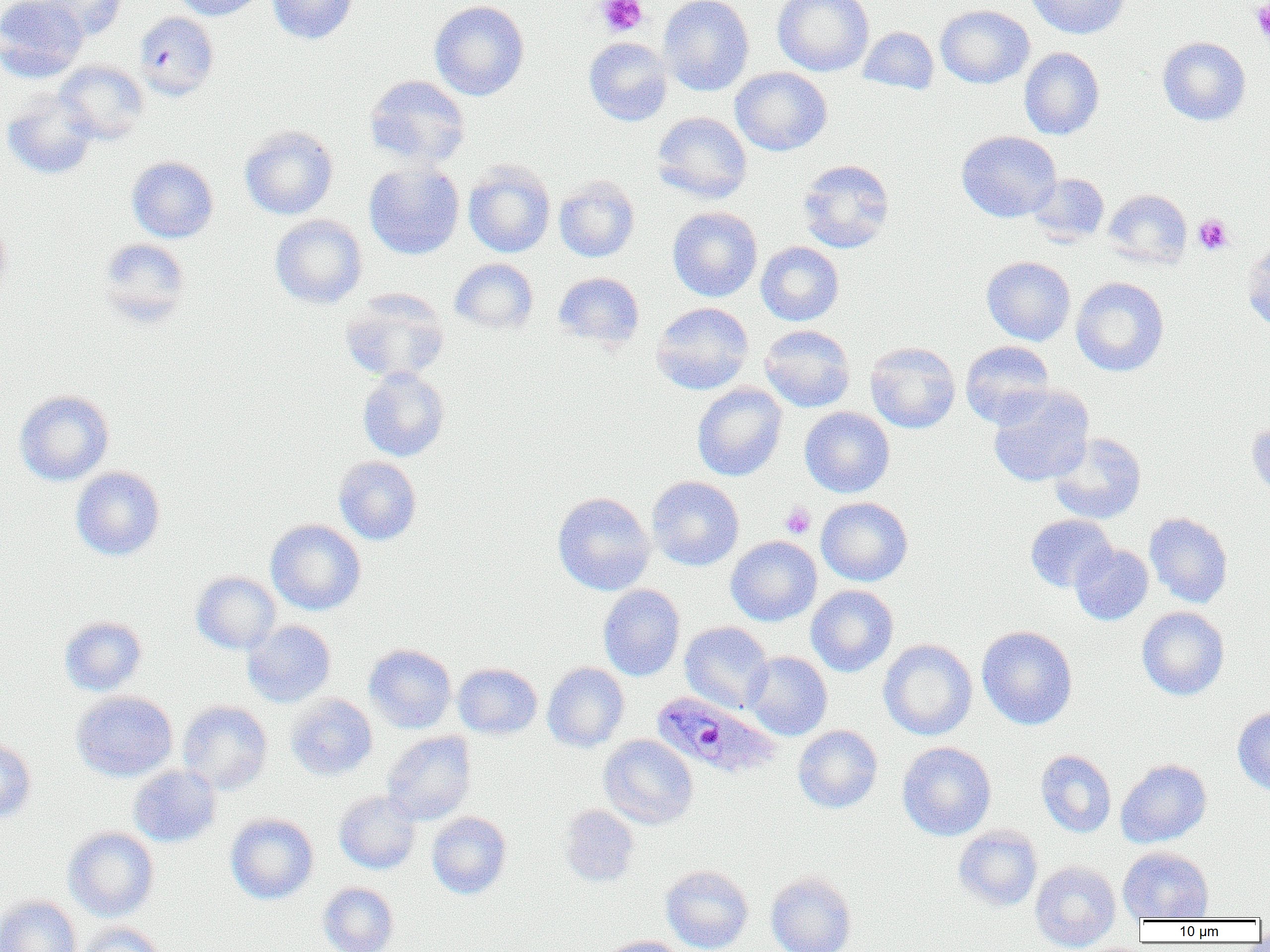
Approximate bounding boxes as (x1,y1)-(x2,y2) corner pairs in pixels. Plasmodium ovale-infected red blood cell locations: (653,691)-(782,779). Platelet locations: (597,0)-(648,37), (1251,1)-(1270,42), (1194,214)-(1232,254), (780,502)-(816,539). Uninfected red blood cell locations: (0,0)-(89,81), (34,0)-(126,40), (171,0)-(267,20), (267,0)-(358,44), (659,0)-(754,96), (773,0)-(874,76), (1026,0)-(1129,39), (429,1)-(530,101), (935,4)-(1034,89), (134,11)-(219,100), (858,26)-(939,94), (583,37)-(673,126), (1157,37)-(1251,126), (1019,48)-(1104,140), (55,61)-(150,144), (730,67)-(832,156), (363,75)-(471,168), (2,88)-(100,180), (652,112)-(752,203), (240,125)-(338,220), (957,131)-(1061,222), (126,156)-(219,243), (797,159)-(895,253), (364,161)-(465,260), (463,161)-(556,258), (1028,173)-(1110,246), (553,174)-(640,262), (1103,189)-(1192,268), (667,206)-(762,302), (269,214)-(368,309), (0,216)-(13,306), (97,238)-(191,326), (1242,240)-(1270,333), (756,242)-(844,326), (981,256)-(1076,345), (449,258)-(539,334), (553,272)-(646,350), (1071,276)-(1169,377), (339,288)-(451,383), (650,302)-(754,394), (759,324)-(855,412), (960,340)-(1056,428), (865,342)-(960,433), (357,368)-(450,462), (691,383)-(787,481), (987,387)-(1094,487), (14,390)-(114,486), (799,407)-(895,498), (1246,418)-(1270,505), (1049,433)-(1146,524), (334,456)-(421,545), (70,467)-(165,561), (647,476)-(744,571), (552,492)-(655,595), (816,497)-(912,586), (1145,513)-(1233,608), (1025,514)-(1116,592), (266,519)-(366,615), (725,536)-(822,626), (1070,542)-(1153,625), (191,571)-(281,654), (598,584)-(685,681), (806,585)-(899,676), (1137,606)-(1229,700), (59,616)-(147,696), (242,620)-(336,707), (680,622)-(773,714), (977,625)-(1078,730), (878,639)-(977,740), (364,644)-(457,733), (743,651)-(832,740), (453,662)-(542,739), (542,662)-(629,752), (72,691)-(177,781), (285,693)-(377,781), (179,699)-(377,786), (177,701)-(272,795), (1232,707)-(1270,795), (793,725)-(883,814), (382,731)-(476,825), (599,734)-(698,829), (0,738)-(36,823), (897,742)-(996,840), (1036,749)-(1116,837), (1116,759)-(1211,847), (128,765)-(221,847), (334,790)-(421,874), (559,804)-(640,887), (426,812)-(512,899), (225,813)-(319,904), (953,825)-(1043,910), (63,826)-(159,921), (1118,847)-(1213,922), (1030,860)-(1121,951), (660,865)-(754,952), (765,871)-(857,952), (318,882)-(398,952), (0,896)-(82,952), (76,923)-(167,952), (597,936)-(689,952). Slide-level diagnosis: Plasmodium ovale. 1000x magnification. Image is 1270×952 pixels. Optical microscopy. Single field of view. Thin blood film.